Outline each blood parasite and name the species.
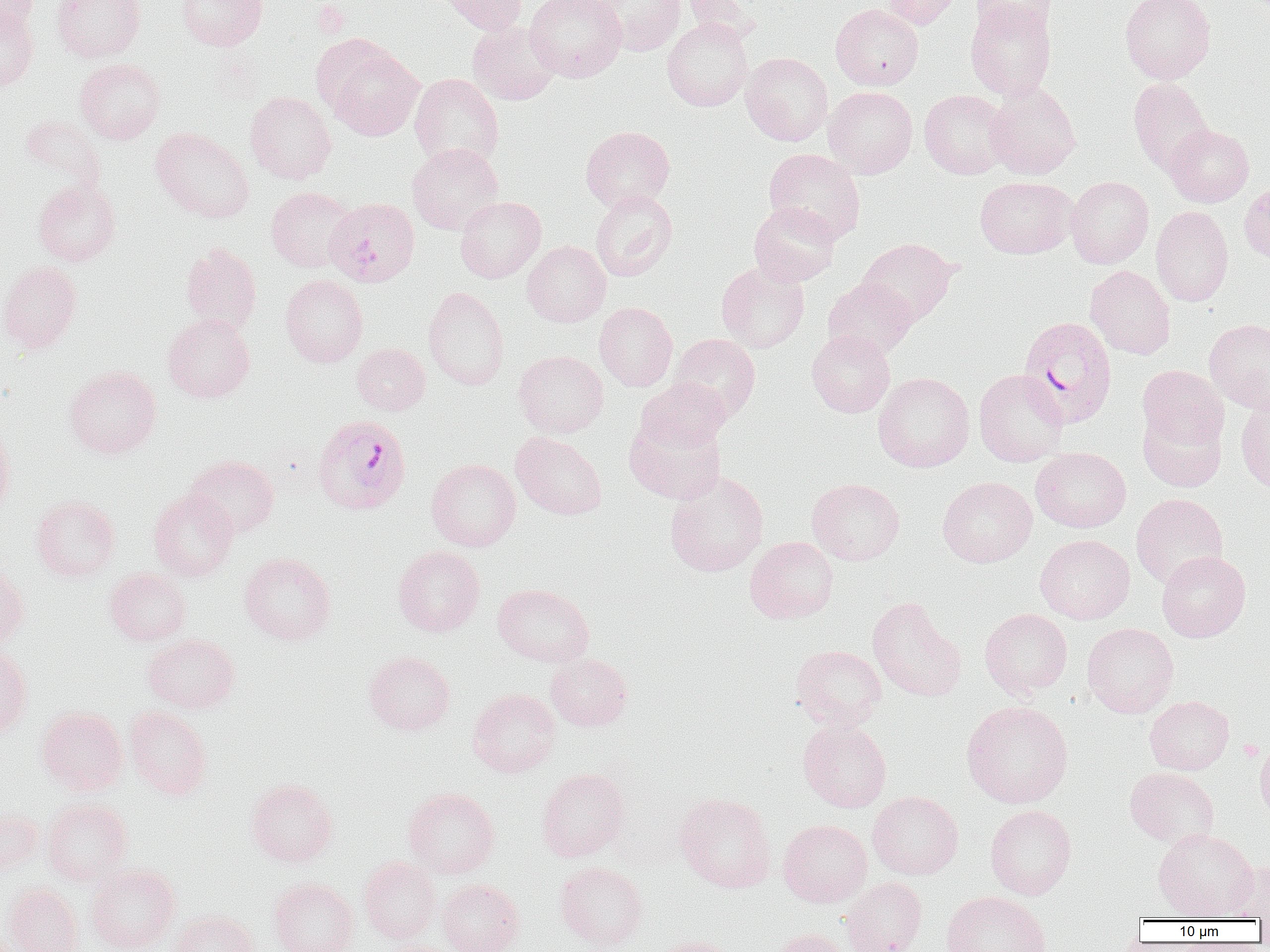

Approximate bounding boxes as (x1,y1)-(x2,y2) corner pairs in pixels.
Plasmodium falciparum-infected red blood cells: (324,197)-(421,287), (1017,315)-(1117,428), (317,419)-(416,520).
No Plasmodium ovale, Plasmodium malariae, Plasmodium vivax, Babesia divergens, or Trypanosoma brucei observed.

slide_level_diagnosis: Plasmodium falciparum
preparation: thin blood smear
uninfected_red_blood_cell_locations: 'approximate bounding boxes as (x1,y1)-(x2,y2) corner pairs in pixels: (0,0)-(38,37), (51,0)-(146,62), (176,0)-(267,50), (436,0)-(528,34), (525,0)-(627,82), (591,0)-(686,56), (682,0)-(760,43), (880,0)-(961,29), (970,0)-(1056,36), (1120,0)-(1216,83), (964,1)-(1056,101), (831,3)-(923,90), (0,5)-(39,91), (662,18)-(753,111), (467,20)-(561,105), (323,40)-(423,141), (741,52)-(833,146), (74,58)-(166,144), (409,73)-(503,169), (1128,78)-(1214,174), (985,83)-(1081,179), (823,86)-(918,178), (919,89)-(1010,179), (245,91)-(336,184), (18,115)-(106,192), (1164,124)-(1254,207), (580,125)-(675,212), (151,128)-(254,223), (407,143)-(503,234), (763,148)-(866,244), (975,176)-(1078,258), (1066,176)-(1154,268), (33,179)-(120,266), (1239,179)-(1270,265), (266,186)-(356,272), (591,189)-(677,281), (455,196)-(545,283), (748,201)-(841,287), (1151,205)-(1233,307), (857,237)-(957,326), (522,241)-(610,327), (180,243)-(262,334), (0,261)-(81,353), (716,261)-(809,353), (1085,265)-(1176,359), (280,274)-(368,367), (823,277)-(918,359), (423,286)-(509,390), (594,302)-(677,391), (162,314)-(254,403), (1204,319)-(1270,414), (806,329)-(895,418), (670,333)-(760,422), (352,343)-(430,415), (514,350)-(608,438), (64,365)-(161,458), (1137,365)-(1229,451), (973,369)-(1069,466), (873,372)-(975,472), (636,378)-(731,453), (1235,398)-(1270,496), (1138,408)-(1227,492), (624,412)-(728,505), (0,420)-(16,518), (511,432)-(607,520), (1031,447)-(1131,533), (184,455)-(279,538), (426,459)-(521,551), (664,470)-(769,577), (937,476)-(1037,567), (807,477)-(905,566), (149,490)-(238,581), (1131,493)-(1228,589), (31,495)-(120,582), (1035,534)-(1135,624), (745,536)-(838,624), (393,545)-(485,637), (1156,551)-(1251,642), (239,552)-(336,645), (0,566)-(29,648), (105,568)-(191,646), (492,583)-(594,667), (867,596)-(967,702), (980,608)-(1073,698), (1082,623)-(1179,717), (143,634)-(239,713), (791,645)-(887,730), (0,646)-(32,737), (363,650)-(455,735), (545,653)-(632,731), (467,688)-(561,777), (1145,695)-(1234,774), (961,700)-(1074,808), (37,706)-(127,795), (124,706)-(213,799), (798,719)-(892,812), (1254,736)-(1270,824), (1125,767)-(1219,848), (537,768)-(630,862), (246,778)-(337,866), (403,787)-(499,878), (867,791)-(963,879), (674,792)-(775,893), (42,798)-(133,885), (985,804)-(1077,900), (0,806)-(43,877), (778,819)-(871,907), (1153,828)-(1258,920), (358,856)-(441,943), (1226,860)-(1270,920), (555,861)-(648,951), (86,863)-(180,952), (269,877)-(358,952), (841,877)-(927,952), (438,879)-(524,952), (3,883)-(84,952), (941,891)-(1051,952), (170,909)-(259,952), (771,928)-(852,952), (650,935)-(741,952)'
field_of_view: single
platelet_locations: 'approximate bounding boxes as (x1,y1)-(x2,y2) corner pairs in pixels: (314,2)-(350,38)'
image_size: 1270×952 pixels
magnification: 1000x
modality: optical microscopy